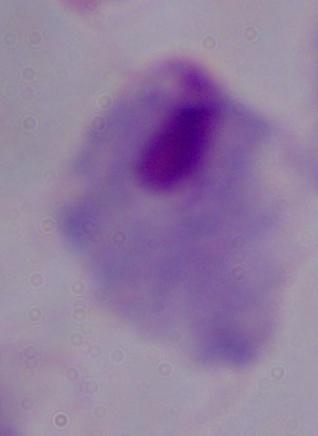
Summary:
  - Magnification: 1000x
  - Identification: trichomonad
  - Modality: micrograph